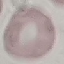
Malaria status: uninfected. Thin blood smear. Acquired by smartphone through the microscope eyepiece. Giemsa-stained preparation. Cell patch, automatically extracted from a larger field of view and resized to 64 × 64 pixels.